State the preparation type.
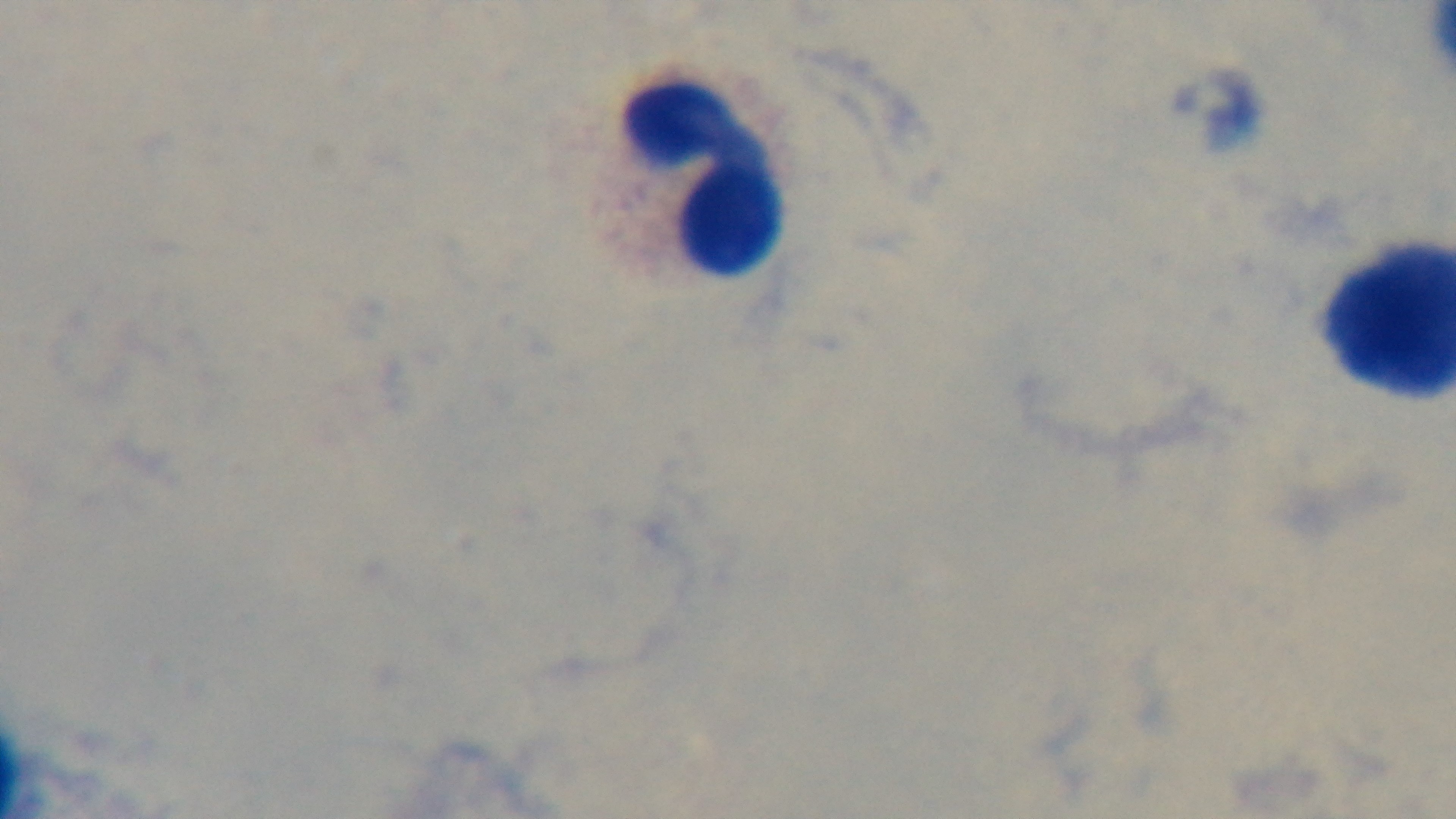
Thick.

malaria_status: negative
objective: 100x oil immersion
capture: mounted 4K digital camera
field_of_view: one from the slide
stain: Giemsa
modality: light microscopy